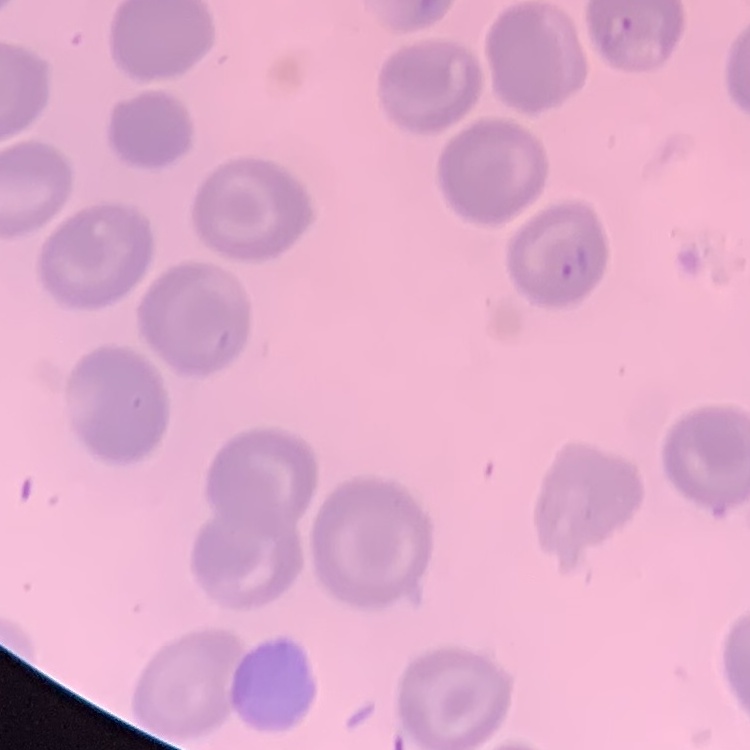

Summary:
  - Erythrocyte morphology: no rouleaux formation
  - Stain: Field's or Giemsa
  - Preparation: thin blood smear
  - Image type: one tile cut from a larger photomicrograph